Locate every Plasmodium vivax-infected red blood cell.
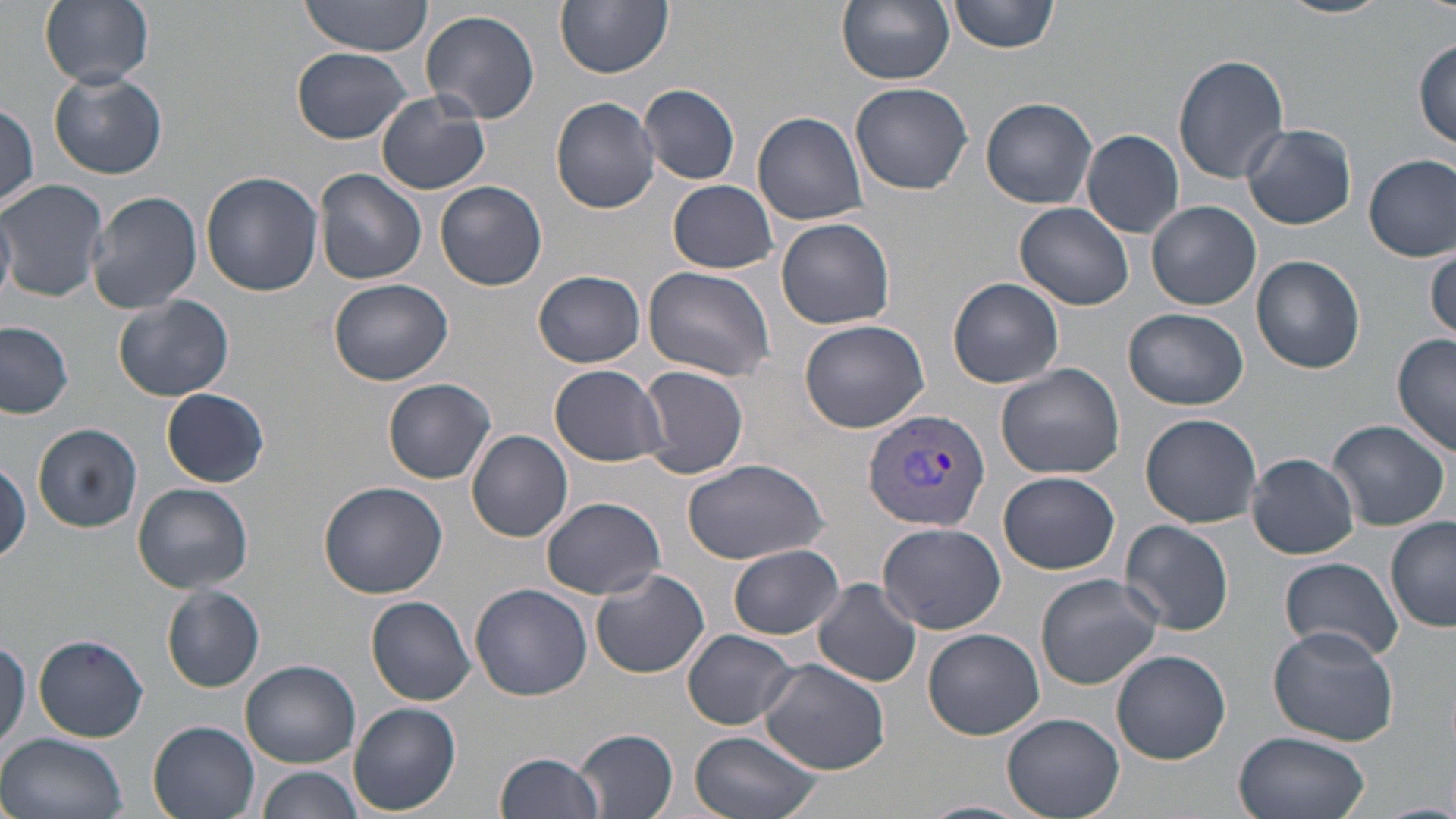

Approximate bounding boxes as (x1, y1, x2, y2) in pixels.
Plasmodium vivax-infected red blood cells: (862, 408, 991, 533).

slide-level diagnosis = Plasmodium vivax
magnification = 1000x
stain = May-Grünwald-Giemsa
modality = optical microscopy
preparation = thin blood smear
uninfected red blood cell locations = approximate bounding boxes as (x1, y1, x2, y2) in pixels: (40, 0, 154, 89), (298, 0, 436, 56), (554, 0, 672, 78), (837, 0, 954, 86), (948, 0, 1057, 54), (1276, 0, 1391, 20), (421, 9, 540, 126), (1413, 39, 1456, 150), (293, 47, 412, 143), (1173, 53, 1290, 183), (49, 71, 167, 180), (850, 82, 973, 196), (639, 83, 741, 184), (376, 91, 489, 195), (551, 97, 662, 213), (980, 98, 1097, 209), (0, 102, 40, 210), (753, 110, 869, 226), (1242, 122, 1357, 230), (1080, 130, 1185, 239), (1365, 154, 1456, 260), (313, 170, 426, 286), (201, 172, 322, 296), (0, 178, 109, 303), (668, 179, 777, 273), (436, 182, 547, 291), (87, 189, 202, 316), (1147, 201, 1261, 311), (1015, 202, 1135, 311), (0, 203, 17, 302), (774, 217, 895, 330), (1425, 244, 1456, 345), (1251, 254, 1366, 374), (644, 266, 776, 382), (533, 270, 647, 368), (328, 277, 455, 386), (947, 277, 1065, 388), (113, 294, 235, 402), (1124, 308, 1248, 411), (0, 320, 75, 419), (798, 320, 930, 434), (1391, 334, 1455, 459), (995, 362, 1125, 479), (550, 364, 670, 465), (638, 364, 749, 478), (383, 377, 496, 485), (162, 387, 271, 486), (1139, 413, 1262, 529), (1326, 419, 1450, 532), (32, 423, 143, 532), (467, 430, 572, 543), (1247, 452, 1360, 559), (680, 457, 829, 564), (0, 459, 30, 565), (999, 471, 1121, 575), (319, 481, 448, 599), (133, 483, 253, 594), (541, 496, 666, 599), (1385, 518, 1455, 634), (1120, 519, 1236, 635), (877, 521, 1006, 636), (728, 544, 843, 640), (1280, 556, 1403, 661), (586, 567, 709, 678), (1033, 573, 1164, 690), (812, 578, 923, 687), (471, 583, 592, 700), (163, 585, 264, 692), (367, 595, 477, 706), (1268, 627, 1397, 747), (923, 628, 1045, 740), (681, 629, 800, 730), (32, 632, 152, 743), (1110, 649, 1232, 765), (758, 657, 893, 774), (241, 660, 360, 767), (349, 703, 461, 814), (1002, 714, 1122, 818), (148, 720, 262, 819), (574, 728, 679, 819), (689, 730, 825, 819), (1234, 730, 1371, 819), (1, 732, 129, 819), (494, 751, 607, 819), (254, 764, 363, 819), (916, 801, 1034, 819)
image size = 1456×819 pixels
field of view = one of a larger specimen